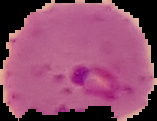
Segmented cell region on a black background. Result: malaria parasites identified. From a thin blood smear. Image is 157×121 pixels.